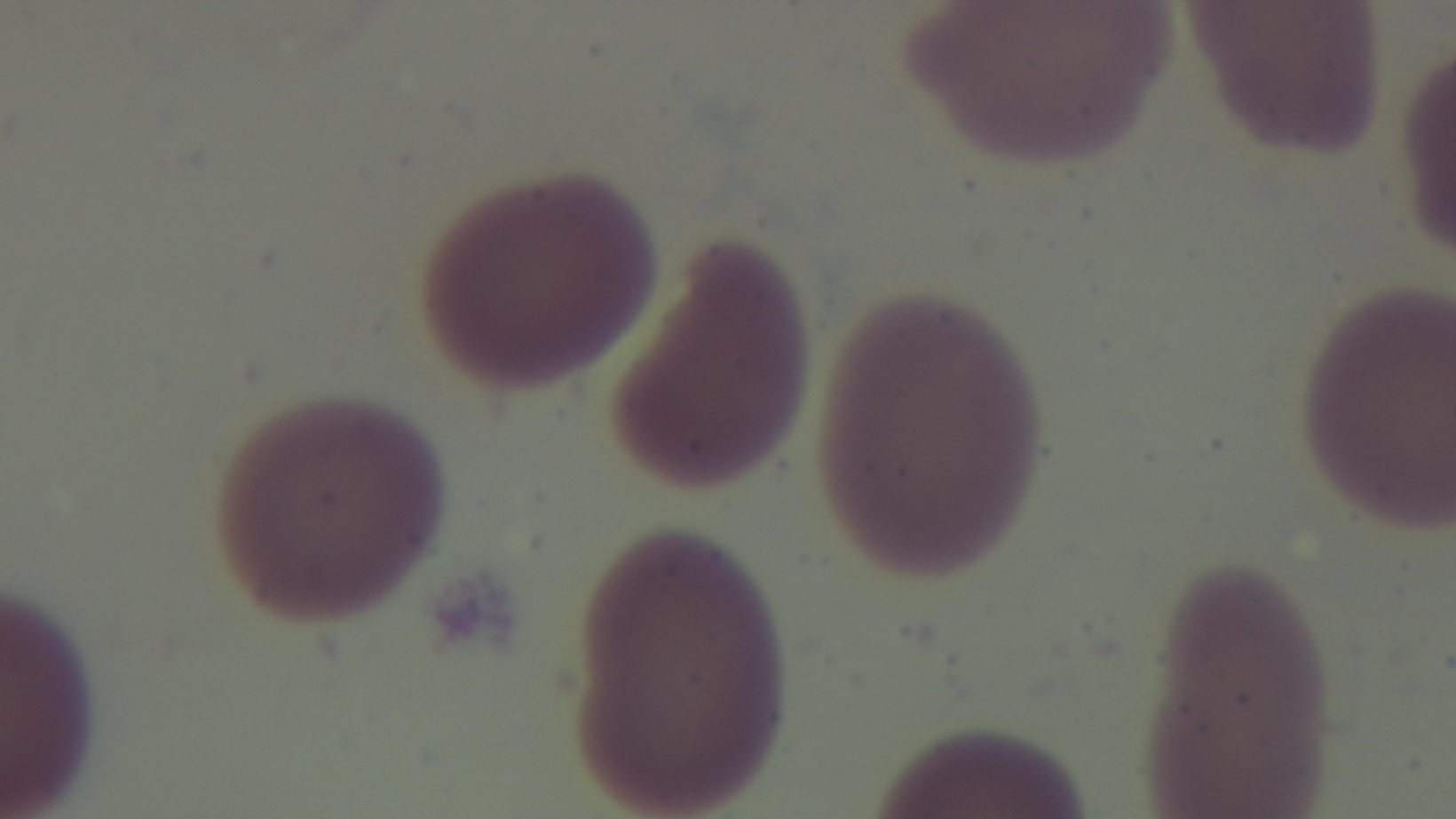
Summary:
  - Objective: 100x oil immersion
  - Preparation: thin smear
  - Stain: Giemsa
  - Field of view: one from the slide
  - Capture: mounted 4K digital camera
  - Modality: light microscopy
  - Malaria status: negative